State the preparation type.
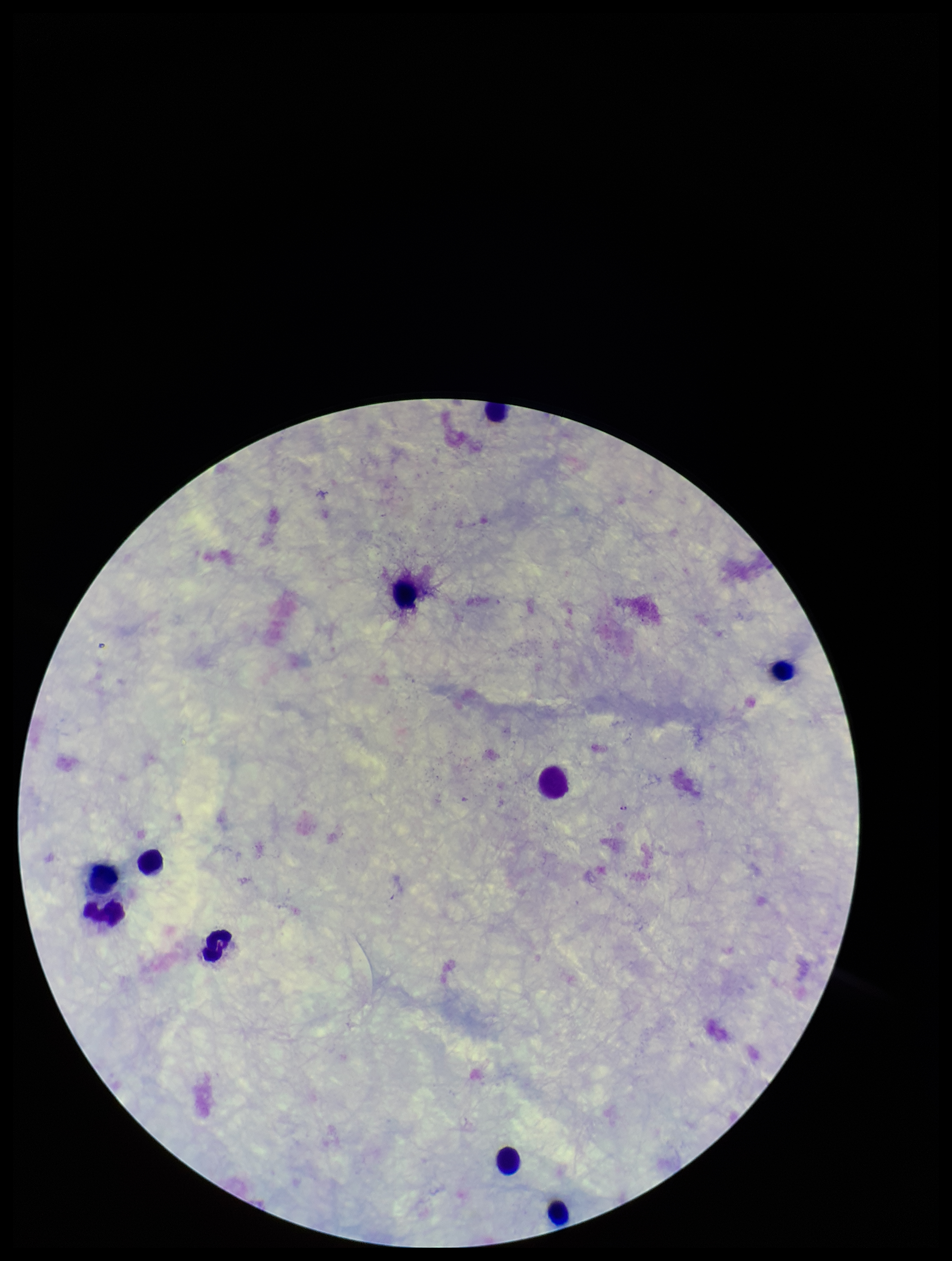
Thick.

Plasmodium parasites = none detected
parasite count = 0
capture = smartphone photograph through the microscope eyepiece
field of view = one from this slide
stain = Giemsa
image size = 952×1261 pixels
leukocyte count = 10
patient malaria status = negative